Report the malaria status of this cell.
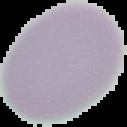
Uninfected.

preparation = thin blood smear
image size = 127×127 pixels
image type = cell region segmented out of the field of view; surrounding area masked to black